Comment on the morphology of the erythrocytes.
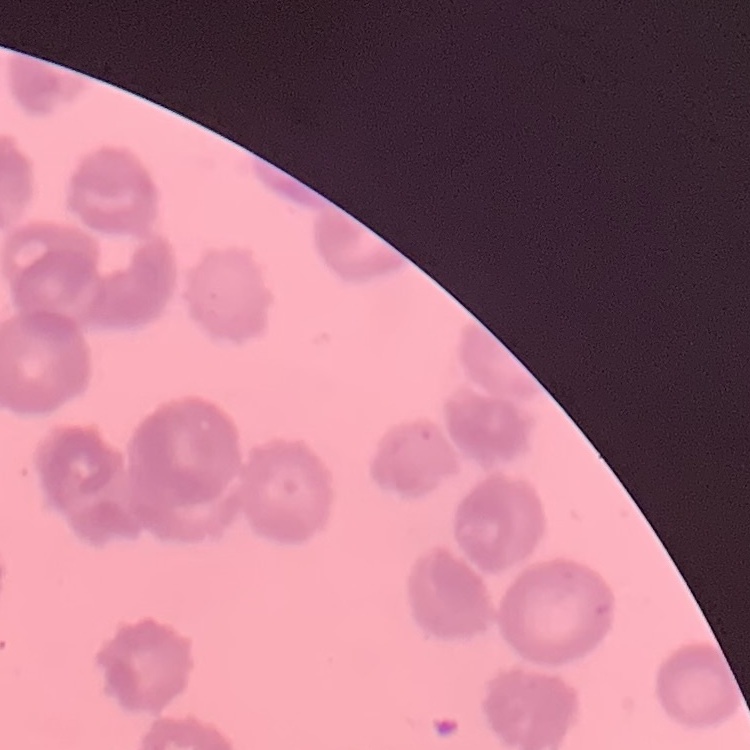

Rouleaux formation.

Thin blood smear. Square crop of a larger photomicrograph. Field's or Giemsa stain.